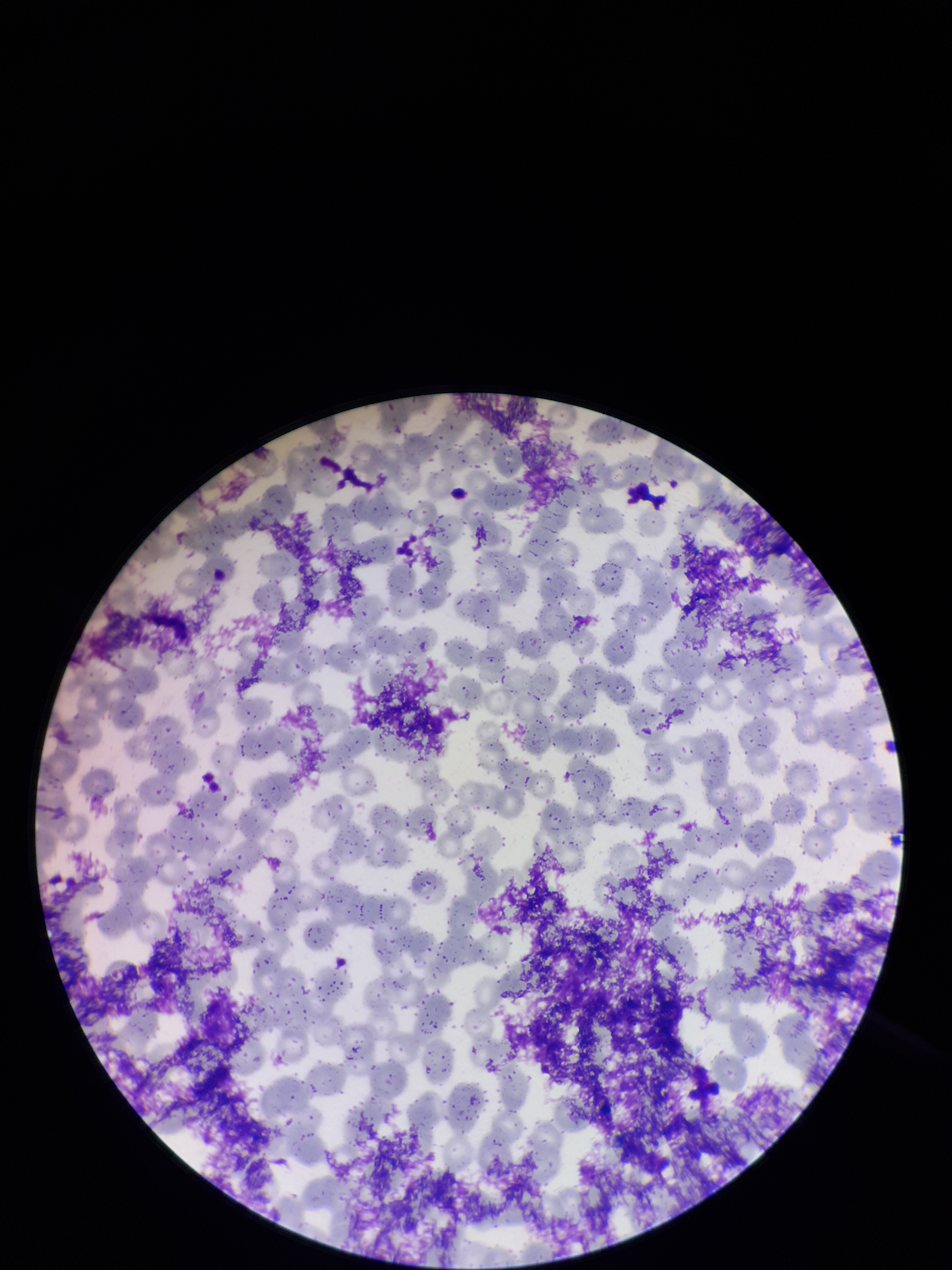
Giemsa stain. Red blood cell count: 303. Parasitized red blood cell count: 0. Preparation: thin smear. Smartphone photograph taken through the eyepiece of a microscope. Image is 952×1270 pixels. Parasitized red blood cells: none detected. One field from this slide. Patient malaria status: negative.